State the blood parasite species.
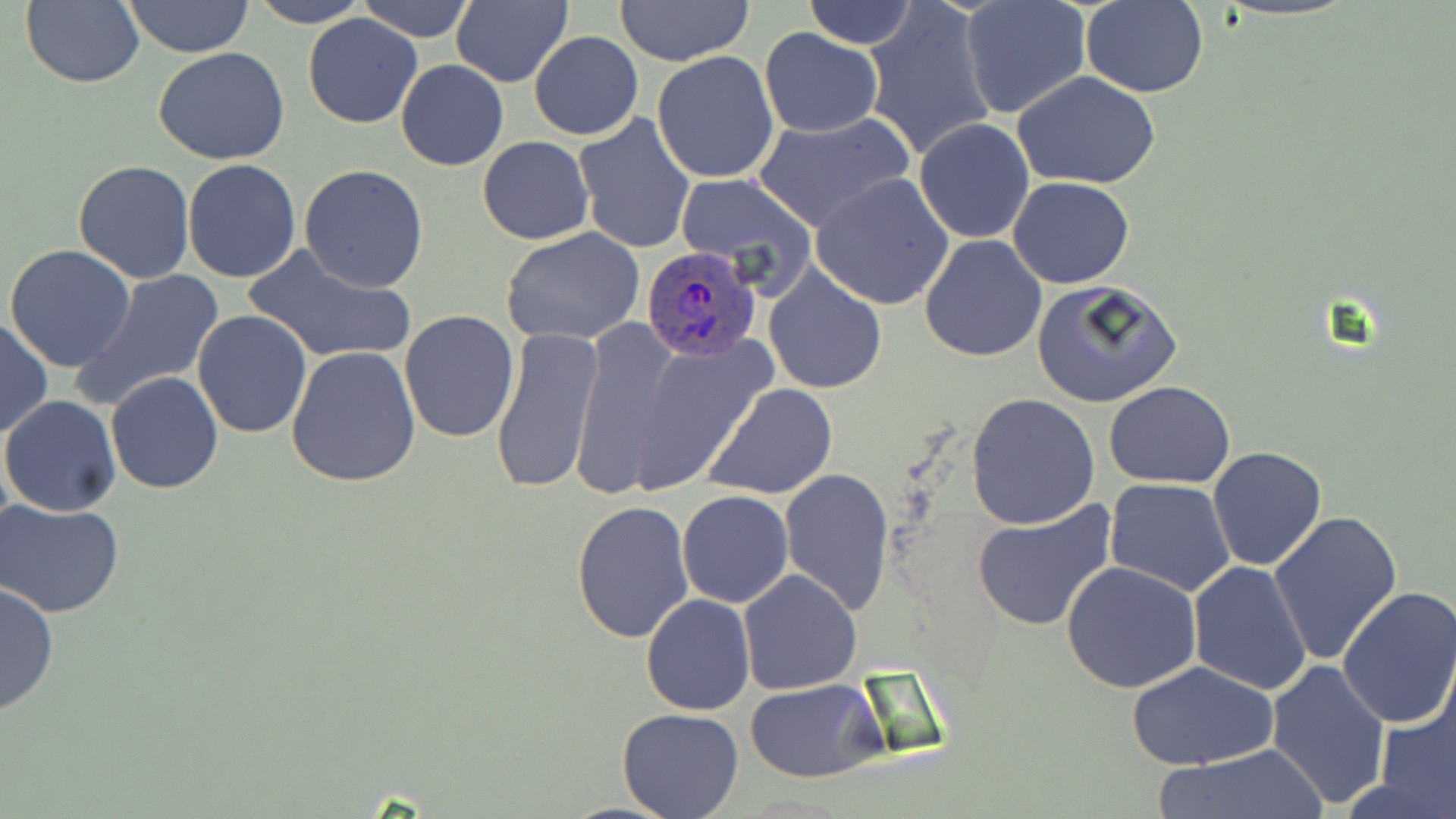

Plasmodium ovale.

Approximate bounding boxes as (x1,y1)-(x2,y2) corner pairs in pixels. Uninfected red blood cell locations: (21,0)-(146,89), (122,0)-(255,58), (247,0)-(368,27), (357,0)-(475,43), (452,0)-(574,89), (612,0)-(756,67), (800,0)-(917,50), (959,1)-(1091,120), (863,2)-(998,163), (1081,2)-(1208,97), (302,12)-(424,128), (758,28)-(884,137), (530,31)-(643,141), (154,47)-(291,165), (652,51)-(779,184), (395,59)-(508,171), (1012,72)-(1162,189), (750,111)-(916,233), (572,113)-(695,254), (913,118)-(1036,244), (477,136)-(593,244), (182,158)-(302,283), (73,159)-(195,284), (299,165)-(429,291), (675,173)-(816,293), (811,173)-(955,309), (1008,176)-(1135,289), (502,227)-(647,349), (918,234)-(1047,363), (244,242)-(415,365), (4,245)-(138,372), (763,265)-(887,395), (76,269)-(228,411), (1030,279)-(1182,408), (399,309)-(519,443), (191,310)-(313,438), (0,316)-(52,439), (567,316)-(690,501), (488,324)-(604,496), (621,330)-(779,492), (285,345)-(422,488), (106,371)-(225,494), (1105,381)-(1235,488), (702,382)-(839,501), (967,392)-(1100,530), (0,394)-(121,516), (1207,447)-(1327,571), (778,466)-(895,616), (1105,479)-(1236,599), (677,490)-(793,608), (571,499)-(695,643), (2,500)-(125,619), (971,501)-(1117,633), (1268,509)-(1403,666), (1061,560)-(1201,694), (1186,561)-(1312,695), (736,569)-(863,696), (0,581)-(58,718), (1335,587)-(1456,730), (640,595)-(755,716), (1126,659)-(1280,769), (1266,659)-(1391,808), (746,680)-(884,782), (1373,687)-(1455,819), (615,708)-(745,819), (1152,747)-(1328,819). Plasmodium ovale-infected red blood cell locations: (638,246)-(763,362). Captured at 1000x magnification. Single field of view. Optical microscopy. May-Grünwald-Giemsa-stained preparation. Thin blood film. Image is 1456×819 pixels.